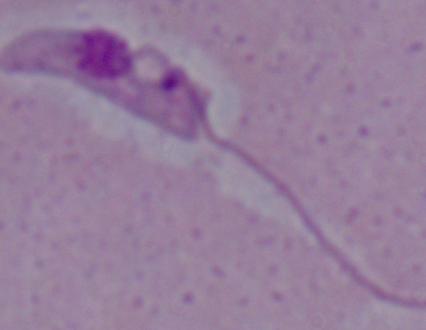
Summary:
  - Magnification: 1000x
  - Modality: micrograph
  - Identification: Leishmania